Classify this cell by malaria status.
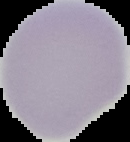
Uninfected.

Summary:
  - Preparation: thin blood film
  - Image type: segmented cell region with the area outside set to black
  - Image size: 130×142 pixels